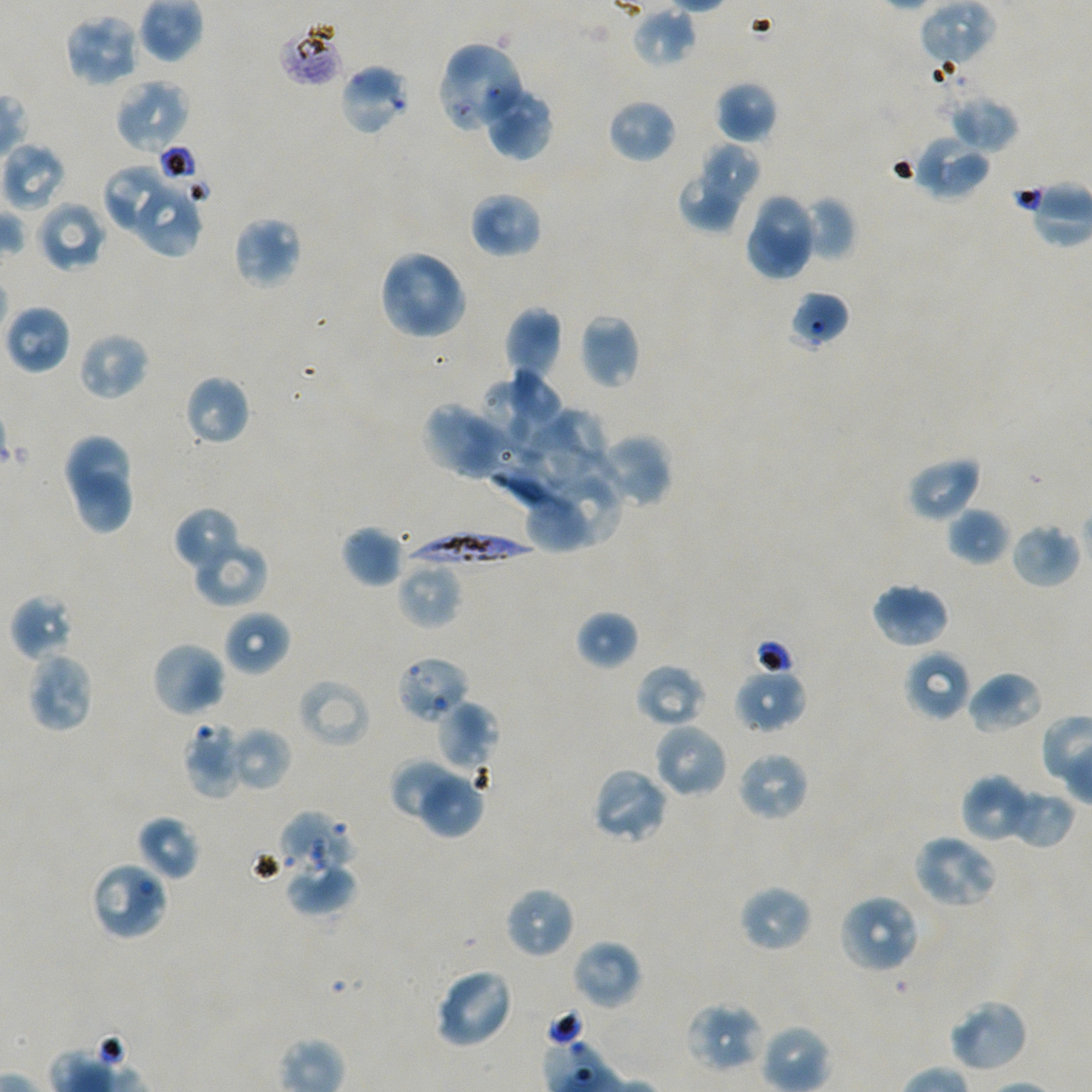

Not every red blood cell is marked.
locations_of_red_blood_cells_of_indeterminate_infection_status: 'approximate bounding boxes as {x1, y1, x2, y2} in pixels: {277, 20, 346, 88}, {448, 41, 526, 121}, {338, 62, 411, 136}, {788, 291, 850, 351}, {395, 655, 471, 725}, {279, 811, 354, 875}, {90, 860, 169, 942}'
field_of_view: single
locations_of_uninfected_red_blood_cells: 'approximate bounding boxes as {x1, y1, x2, y2} in pixels: {920, 0, 997, 66}, {631, 5, 697, 67}, {64, 13, 141, 88}, {114, 77, 191, 154}, {713, 81, 779, 143}, {482, 84, 554, 162}, {947, 93, 1019, 153}, {607, 98, 677, 164}, {913, 134, 990, 202}, {1, 141, 68, 212}, {700, 142, 761, 204}, {103, 166, 172, 232}, {680, 172, 742, 231}, {138, 188, 202, 259}, {469, 191, 543, 259}, {755, 193, 814, 264}, {799, 196, 856, 262}, {35, 200, 107, 272}, {232, 215, 302, 290}, {748, 221, 808, 278}, {378, 250, 467, 341}, {3, 304, 72, 375}, {503, 306, 563, 380}, {579, 313, 640, 389}, {77, 331, 149, 401}, {513, 365, 562, 427}, {184, 374, 251, 446}, {483, 383, 530, 449}, {421, 401, 510, 479}, {554, 406, 609, 461}, {520, 424, 583, 488}, {602, 434, 672, 507}, {66, 435, 130, 502}, {906, 455, 982, 522}, {75, 472, 130, 531}, {559, 475, 622, 545}, {527, 496, 583, 554}, {173, 507, 243, 575}, {947, 507, 1010, 566}, {1009, 523, 1080, 589}, {340, 526, 402, 587}, {194, 539, 268, 607}, {397, 559, 462, 630}, {869, 581, 951, 649}, {10, 594, 75, 662}, {222, 609, 291, 676}, {575, 610, 640, 671}, {151, 640, 227, 718}, {903, 649, 972, 721}, {24, 651, 95, 733}, {634, 663, 706, 727}, {733, 667, 807, 733}, {966, 670, 1044, 735}, {296, 678, 372, 749}, {437, 700, 498, 771}, {183, 722, 243, 799}, {653, 722, 728, 799}, {228, 727, 292, 792}, {736, 750, 810, 822}, {391, 758, 459, 820}, {590, 766, 670, 845}, {418, 774, 487, 839}, {960, 774, 1025, 841}, {1002, 789, 1076, 849}, {136, 815, 200, 881}, {912, 833, 1000, 910}, {285, 861, 355, 915}, {738, 884, 814, 953}, {503, 886, 576, 960}, {838, 893, 921, 975}, {570, 939, 643, 1011}, {433, 966, 515, 1050}, {947, 998, 1030, 1074}, {685, 1001, 767, 1073}'
preparation: thin blood smear
locations_of_infected_red_blood_cells: 'approximate bounding boxes as {x1, y1, x2, y2} in pixels: {440, 65, 510, 130}, {405, 528, 533, 568}'
donor_blood_group: A+/O+
objective: 100x, oil immersion, numerical aperture 1.45
culture: static in-vitro Plasmodium falciparum strain NF54
stain: Giemsa
image_size: 1092×1092 pixels